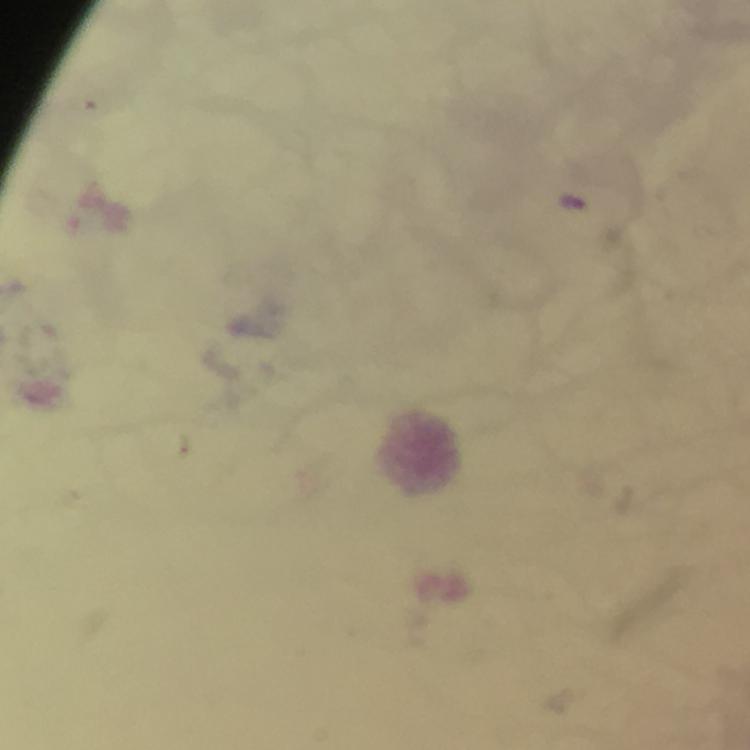

preparation = thick smear
context = from a diagnostic examination for malaria
image size = 750×750 pixels
cropped from = one field of view
malaria parasite locations = approximate centers as [x, y] in pixels: [574, 202]
capture = smartphone photograph through a microscope
immersion oil = used
stain = Giemsa
magnification = 100x